Report the malaria status of this cell.
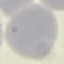
Uninfected.

Summary:
  - Stain: Giemsa
  - Image type: cell patch, automatically extracted from a larger field of view and resized to 64 × 64 pixels
  - Capture: smartphone camera at the microscope eyepiece
  - Preparation: thin smear